Classify this cell by malaria status.
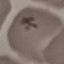
Uninfected.

Automatically extracted cell patch, resized to 64 × 64 pixels. Thin blood smear. Giemsa stain. Photographed with a smartphone camera at the microscope eyepiece.